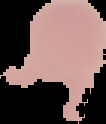
{
  "preparation": "thin blood smear",
  "result": "negative for malaria parasites",
  "image_type": "cell region segmented out of the field of view; surrounding area masked to black",
  "image_size": "106×124 pixels"
}